Assess this cell for malaria.
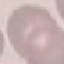
Uninfected.

Summary:
  - Stain: Giemsa
  - Preparation: thin blood smear
  - Image type: automatically extracted cell patch, resized to 64 × 64 pixels
  - Capture: smartphone camera at the microscope eyepiece